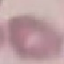

result = no malaria parasites seen
capture = smartphone camera at the microscope eyepiece
image type = cell patch, automatically extracted from a larger field of view and resized to 64 × 64 pixels
preparation = thin smear
stain = Giemsa